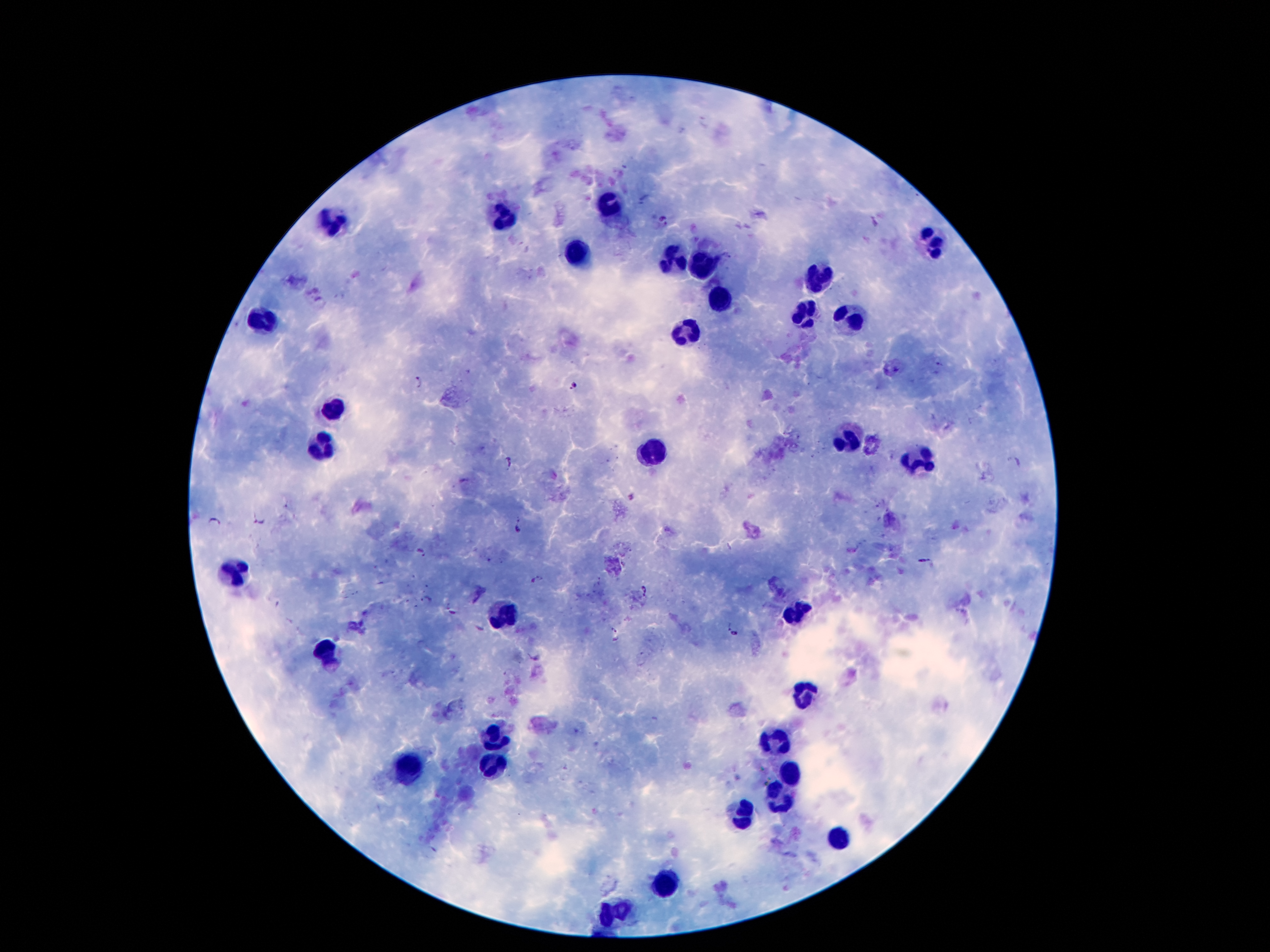
malaria_parasite_locations: 'approximate centers as [x, y] in pixels: [663, 222], [897, 370], [417, 382], [573, 386], [510, 462], [1016, 462], [214, 520], [260, 521], [520, 524], [420, 550], [922, 559], [536, 580], [645, 590], [427, 599], [450, 612], [734, 634], [616, 635], [536, 658]'
leukocyte_locations: 'approximate centers as [x, y] in pixels: [612, 205], [506, 217], [332, 221], [934, 242], [578, 254], [676, 262], [703, 266], [819, 275], [721, 305], [805, 312], [852, 318], [260, 324], [688, 332], [334, 408], [846, 435], [324, 443], [649, 453], [914, 459], [233, 570], [500, 611], [795, 613], [326, 654], [807, 691], [492, 734], [776, 744], [494, 760], [410, 773], [793, 777], [780, 793], [743, 812], [840, 840], [666, 885], [616, 910]'
magnification: 100x
preparation: thick blood film
patient_malaria_status: positive for Plasmodium falciparum
capture: smartphone camera through the microscope eyepiece
stain: Giemsa
image_size: 1270×952 pixels
field_of_view: one from this slide